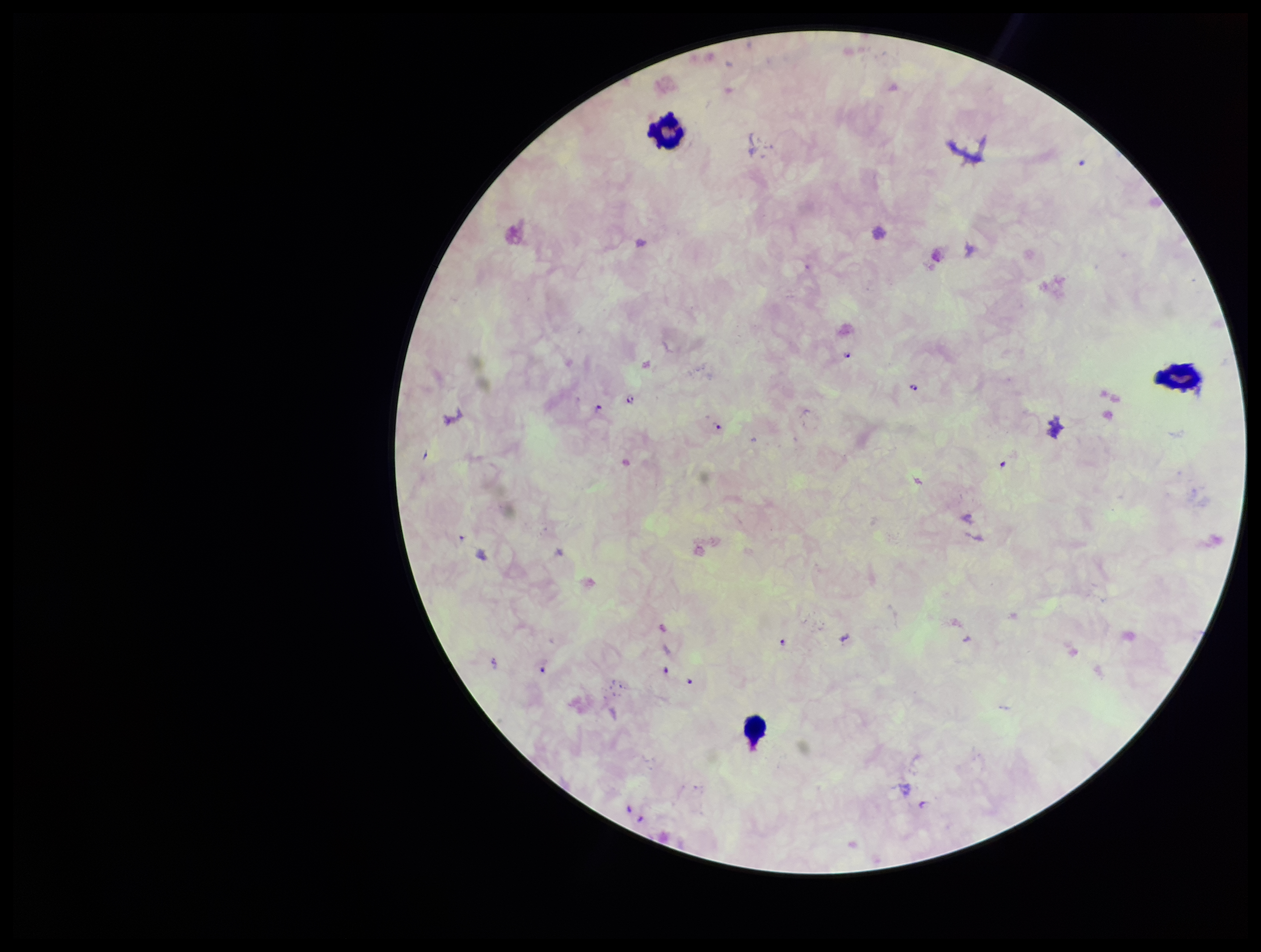
Summary:
  - Species reported for this patient: Plasmodium falciparum
  - Field of view: single
  - Parasite count: 10
  - Leukocyte count: 3
  - Image size: 1261×952 pixels
  - Capture: smartphone photograph through the microscope eyepiece
  - Patient malaria status: positive
  - Stain: Giemsa
  - Preparation: thick blood smear
  - Plasmodium parasites: identified